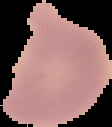

image size = 112×127 pixels
malaria status = uninfected
image type = segmented cell region with the area outside set to black
preparation = thin blood film